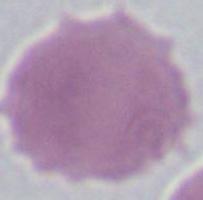
A red blood cell is shown. Photomicrograph. 1000x magnification.